Point out each Plasmodium parasite.
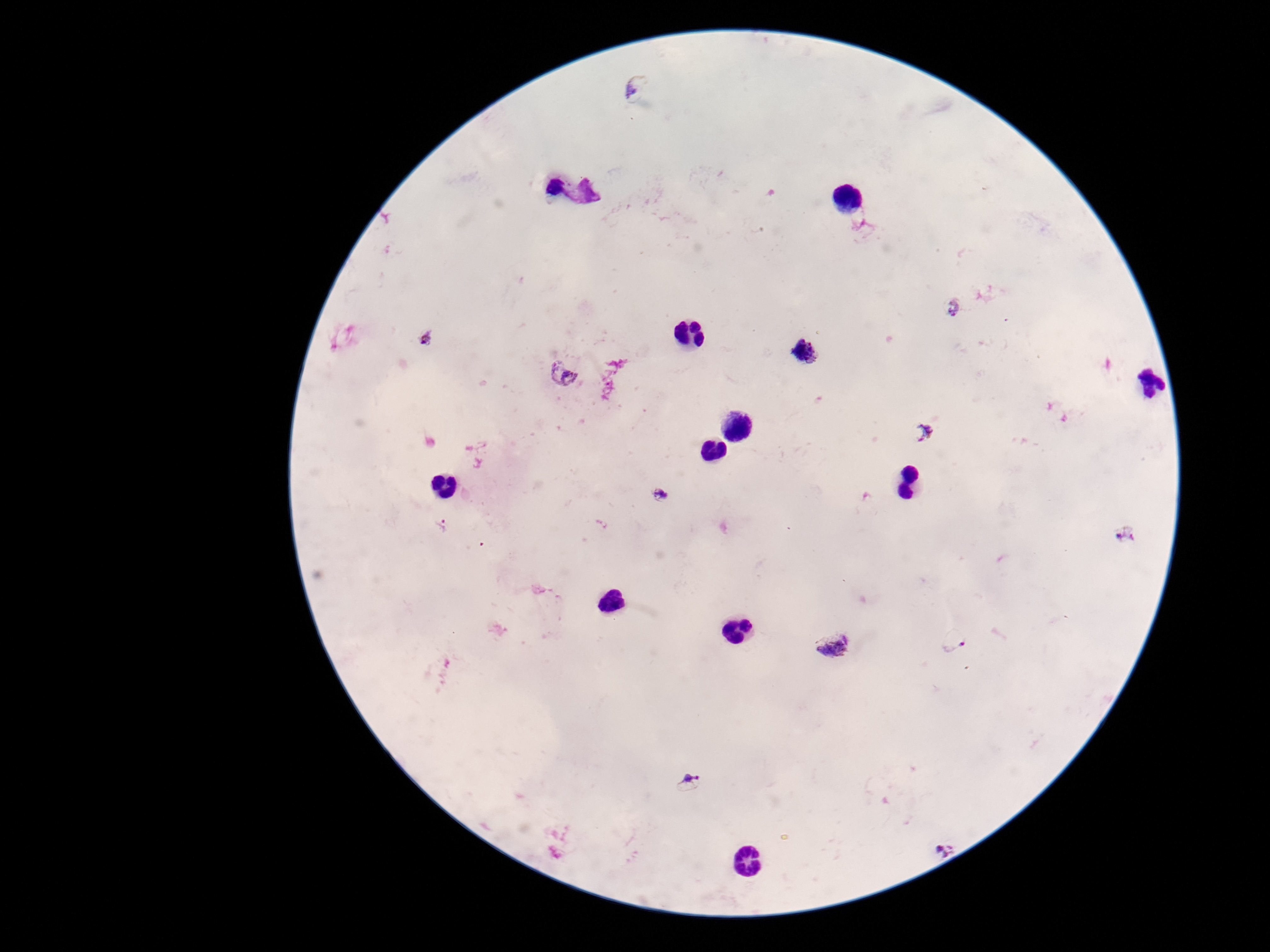
Approximate centers as (x, y) in pixels.
Plasmodium parasites: (638, 88), (952, 306), (427, 337), (804, 350), (561, 374), (924, 433), (661, 497), (441, 524), (1125, 535), (953, 642), (832, 643), (689, 783), (942, 848).

100x magnification. Patient malaria status: infected. Giemsa-stained preparation. Single field of view. Thick peripheral-blood smear. Image is 1270×952 pixels. Photographed through the microscope eyepiece with a smartphone camera.